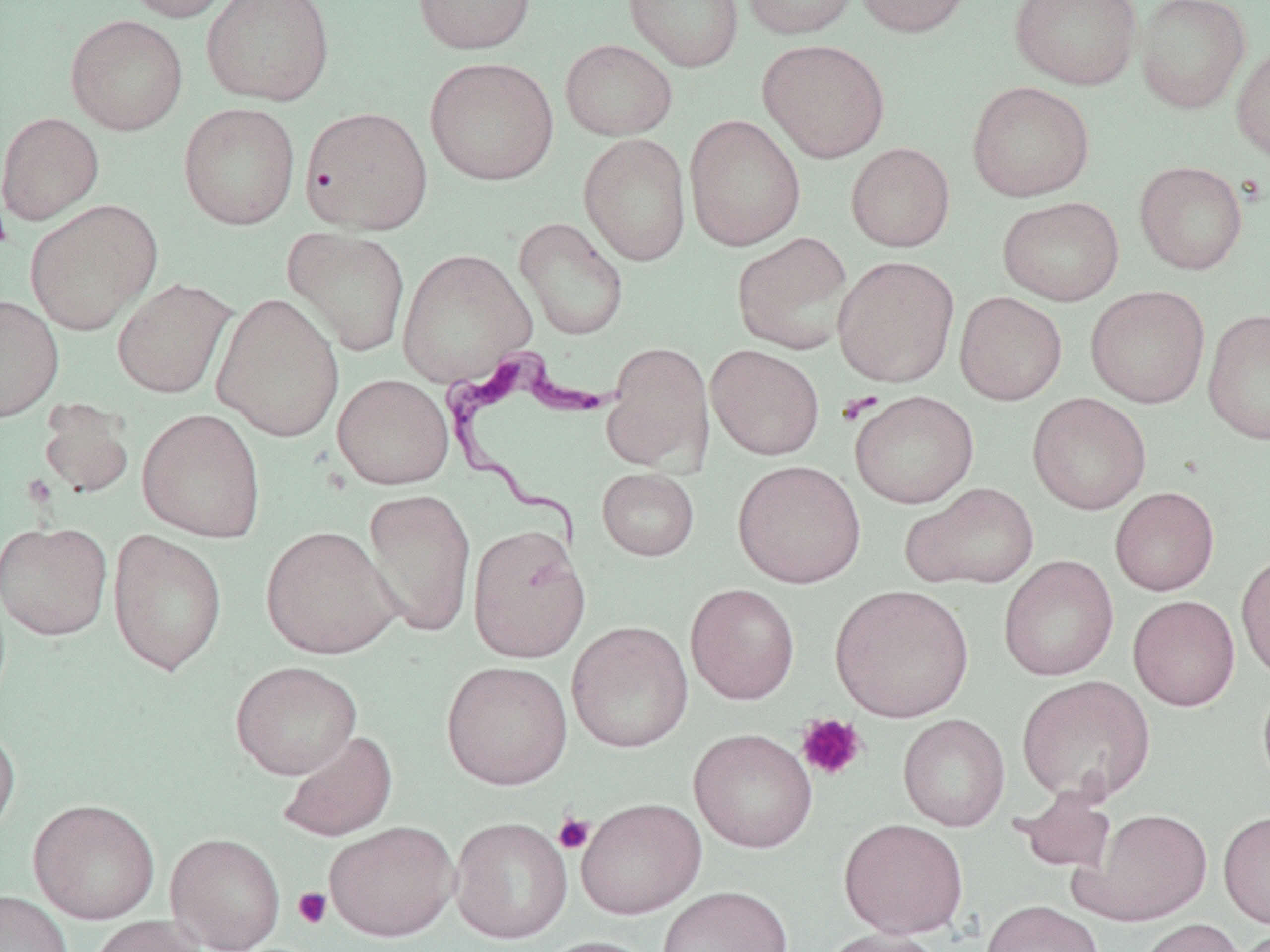

Summary:
  - Coordinate format: approximate bounding boxes as named x1/y1/x2/y2 corners in pixels
  - Platelet locations: (x1=0, y1=201, x2=12, y2=254), (x1=837, y1=391, x2=884, y2=425), (x1=796, y1=713, x2=867, y2=781), (x1=553, y1=812, x2=595, y2=854), (x1=293, y1=887, x2=332, y2=929)
  - Trypanosoma brucei locations: (x1=440, y1=348, x2=614, y2=558)
  - Uninfected red blood cell locations: (x1=123, y1=0, x2=242, y2=23), (x1=201, y1=0, x2=335, y2=106), (x1=412, y1=0, x2=536, y2=55), (x1=623, y1=0, x2=744, y2=72), (x1=740, y1=0, x2=860, y2=39), (x1=854, y1=0, x2=975, y2=37), (x1=1009, y1=0, x2=1142, y2=90), (x1=1135, y1=0, x2=1251, y2=114), (x1=65, y1=14, x2=188, y2=136), (x1=560, y1=38, x2=677, y2=141), (x1=757, y1=38, x2=891, y2=163), (x1=1231, y1=39, x2=1270, y2=163), (x1=424, y1=56, x2=559, y2=186), (x1=966, y1=80, x2=1095, y2=202), (x1=178, y1=102, x2=300, y2=230), (x1=300, y1=106, x2=433, y2=235), (x1=0, y1=112, x2=104, y2=225), (x1=684, y1=114, x2=806, y2=251), (x1=579, y1=133, x2=691, y2=266), (x1=846, y1=143, x2=955, y2=252), (x1=1134, y1=160, x2=1248, y2=275), (x1=997, y1=196, x2=1125, y2=306), (x1=25, y1=199, x2=162, y2=335), (x1=514, y1=216, x2=629, y2=341), (x1=283, y1=227, x2=411, y2=357), (x1=732, y1=231, x2=854, y2=354), (x1=396, y1=248, x2=536, y2=387), (x1=832, y1=255, x2=959, y2=387), (x1=112, y1=277, x2=236, y2=399), (x1=1086, y1=285, x2=1210, y2=408), (x1=955, y1=291, x2=1067, y2=405), (x1=211, y1=293, x2=345, y2=442), (x1=0, y1=295, x2=64, y2=423), (x1=1203, y1=307, x2=1270, y2=446), (x1=601, y1=342, x2=714, y2=473), (x1=706, y1=344, x2=825, y2=460), (x1=333, y1=373, x2=454, y2=490), (x1=850, y1=390, x2=979, y2=508), (x1=1027, y1=393, x2=1152, y2=515), (x1=37, y1=400, x2=135, y2=499), (x1=137, y1=408, x2=267, y2=543), (x1=733, y1=459, x2=866, y2=588), (x1=597, y1=468, x2=699, y2=561), (x1=903, y1=482, x2=1039, y2=590), (x1=1110, y1=486, x2=1220, y2=595), (x1=361, y1=488, x2=476, y2=637), (x1=0, y1=520, x2=113, y2=641), (x1=467, y1=523, x2=590, y2=663), (x1=260, y1=525, x2=402, y2=660), (x1=107, y1=530, x2=228, y2=675), (x1=1236, y1=551, x2=1270, y2=683), (x1=998, y1=555, x2=1119, y2=682), (x1=685, y1=583, x2=800, y2=704), (x1=829, y1=584, x2=975, y2=722), (x1=1128, y1=595, x2=1240, y2=710), (x1=566, y1=620, x2=694, y2=753), (x1=230, y1=660, x2=362, y2=780), (x1=441, y1=660, x2=572, y2=790), (x1=1016, y1=674, x2=1155, y2=805), (x1=1257, y1=678, x2=1270, y2=791), (x1=898, y1=714, x2=1010, y2=831), (x1=0, y1=722, x2=21, y2=843), (x1=688, y1=728, x2=817, y2=854), (x1=277, y1=730, x2=398, y2=842), (x1=1012, y1=787, x2=1116, y2=875), (x1=575, y1=797, x2=707, y2=920), (x1=28, y1=798, x2=160, y2=924), (x1=1077, y1=807, x2=1213, y2=925), (x1=1218, y1=809, x2=1270, y2=928), (x1=450, y1=816, x2=572, y2=944), (x1=838, y1=818, x2=969, y2=939), (x1=325, y1=820, x2=460, y2=941), (x1=165, y1=832, x2=286, y2=951), (x1=657, y1=886, x2=793, y2=952), (x1=0, y1=890, x2=75, y2=952), (x1=981, y1=900, x2=1105, y2=952), (x1=87, y1=915, x2=205, y2=952), (x1=1133, y1=918, x2=1247, y2=952), (x1=815, y1=927, x2=949, y2=952), (x1=1230, y1=928, x2=1270, y2=952), (x1=532, y1=935, x2=662, y2=952)
  - Slide-level diagnosis: Trypanosoma brucei
  - Image size: 1270×952 pixels
  - Modality: optical microscopy
  - Stain: May-Grünwald-Giemsa
  - Preparation: thin blood smear
  - Field of view: single
  - Magnification: 1000x